Assess this cell for malaria.
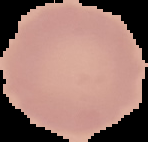
It is uninfected.

{
  "image_size": "148×142 pixels",
  "preparation": "thin blood smear",
  "image_type": "cell region segmented out of the field of view; surrounding area masked to black"
}